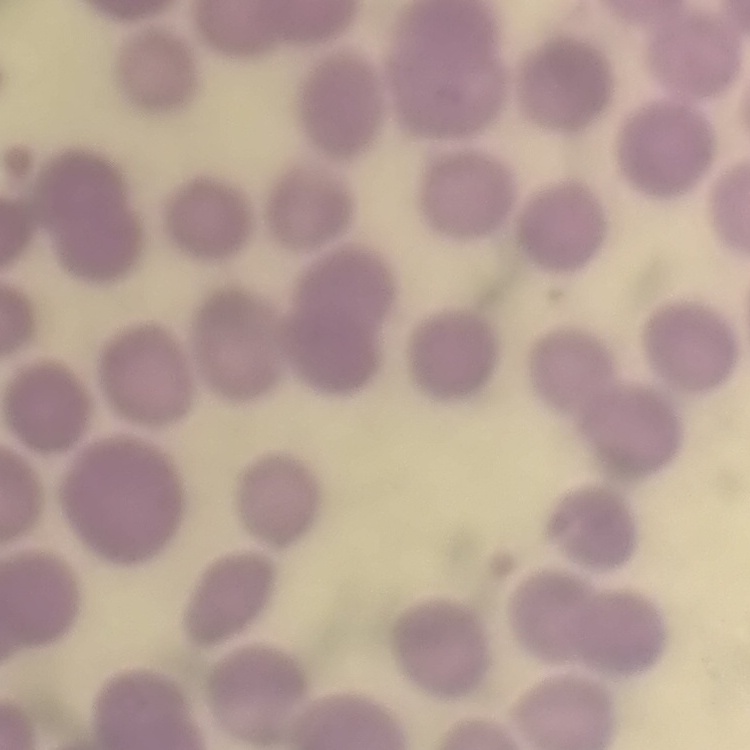

The red blood cells show no rouleaux formation. Thin blood smear. Square crop of a larger photomicrograph. Stained with either Field's or Giemsa.